Report the malaria status of this cell.
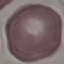

Uninfected.

image type = cell patch, automatically extracted from a larger field of view and resized to 64 × 64 pixels
stain = Giemsa
preparation = thin blood film
capture = smartphone through the microscope eyepiece